Name the blood parasite species.
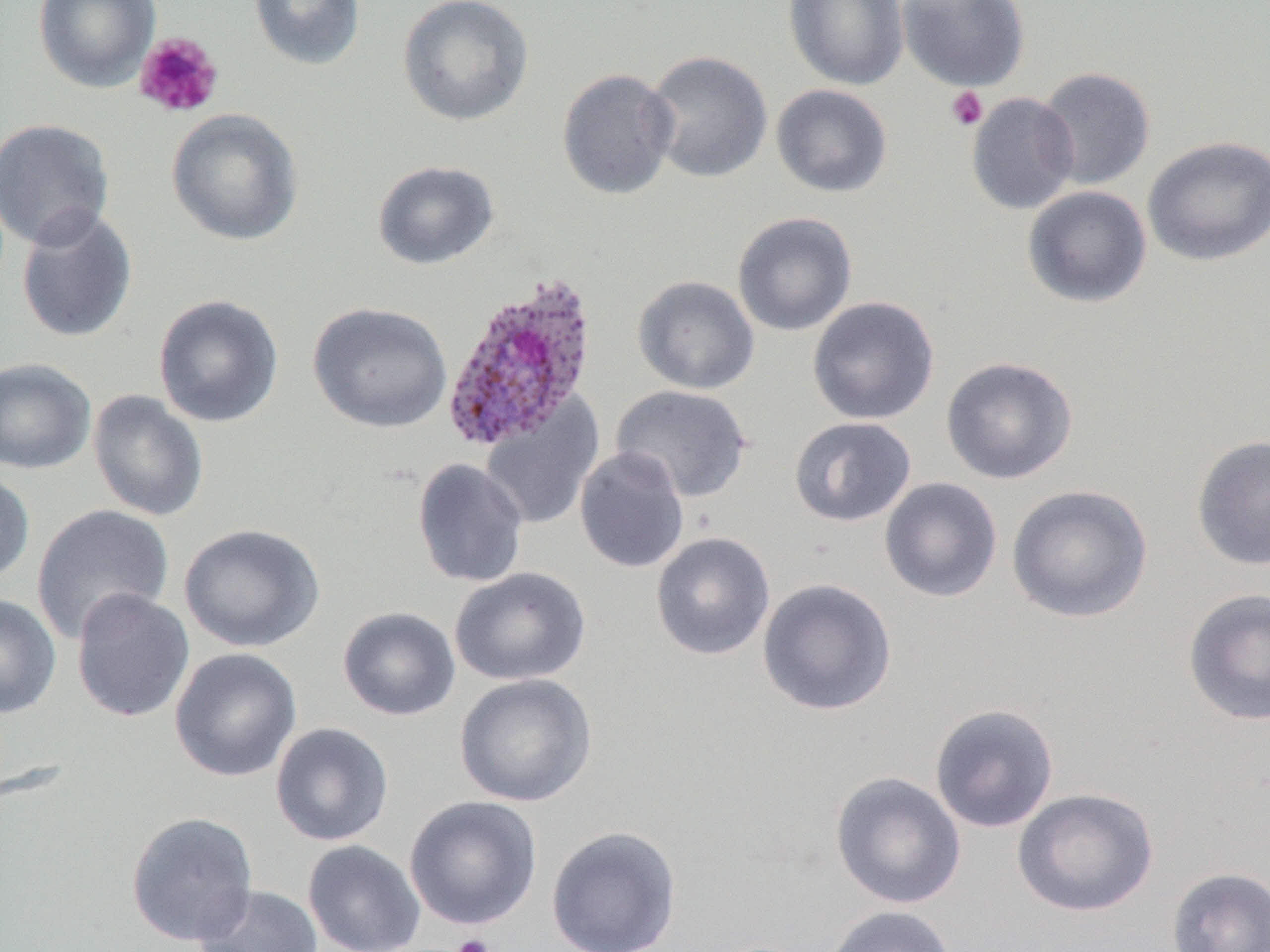

Plasmodium ovale.

Approximate bounding boxes as (x1, y1, x2, y2) in pixels. Platelet locations: (133, 31, 224, 119), (946, 86, 988, 131), (451, 934, 494, 952). Uninfected red blood cell locations: (33, 0, 161, 93), (248, 0, 366, 71), (395, 0, 535, 128), (783, 0, 910, 91), (896, 0, 1031, 92), (643, 50, 773, 185), (1036, 67, 1155, 191), (556, 68, 679, 201), (771, 84, 893, 198), (966, 93, 1079, 215), (166, 108, 305, 247), (0, 117, 116, 251), (1142, 136, 1270, 266), (371, 159, 500, 271), (1021, 185, 1152, 309), (15, 205, 139, 344), (732, 212, 858, 336), (632, 275, 760, 395), (152, 294, 285, 429), (807, 296, 940, 425), (307, 301, 453, 434), (940, 356, 1078, 484), (0, 357, 97, 474), (610, 384, 753, 503), (87, 389, 209, 522), (481, 399, 603, 530), (788, 416, 916, 527), (1191, 435, 1270, 570), (574, 447, 690, 573), (411, 458, 529, 588), (0, 468, 35, 586), (879, 477, 1002, 603), (1006, 484, 1153, 623), (30, 503, 175, 645), (178, 523, 325, 653), (650, 532, 775, 660), (449, 567, 592, 686), (757, 579, 897, 716), (1183, 588, 1270, 726), (71, 589, 194, 723), (0, 593, 62, 719), (337, 606, 461, 721), (169, 647, 302, 783), (454, 672, 598, 808), (929, 703, 1059, 833), (270, 722, 394, 847), (829, 771, 966, 910), (1012, 787, 1158, 917), (404, 795, 543, 930), (125, 810, 258, 947), (546, 824, 682, 952), (302, 839, 426, 952), (1167, 866, 1270, 952), (192, 884, 324, 952), (820, 905, 957, 952). Plasmodium ovale-infected red blood cell locations: (440, 273, 600, 453). Thin blood film. Captured at 1000x magnification. One field of a larger specimen. Image is 1270×952 pixels. Light microscopy.